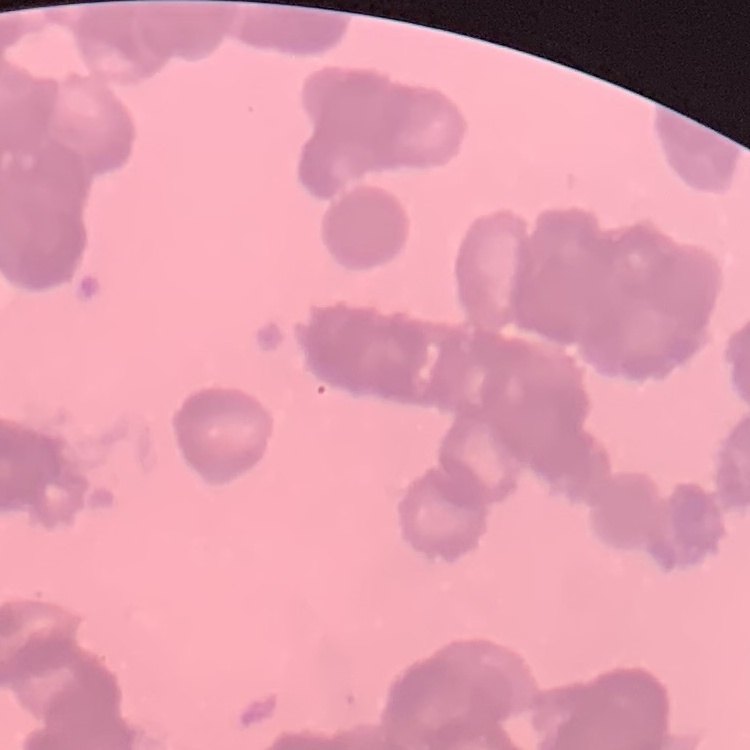

red blood cell morphology = rouleaux formation
image type = one tile cut from a larger photomicrograph
stain = Field's or Giemsa
preparation = thin peripheral smear